Locate and identify every blood parasite.
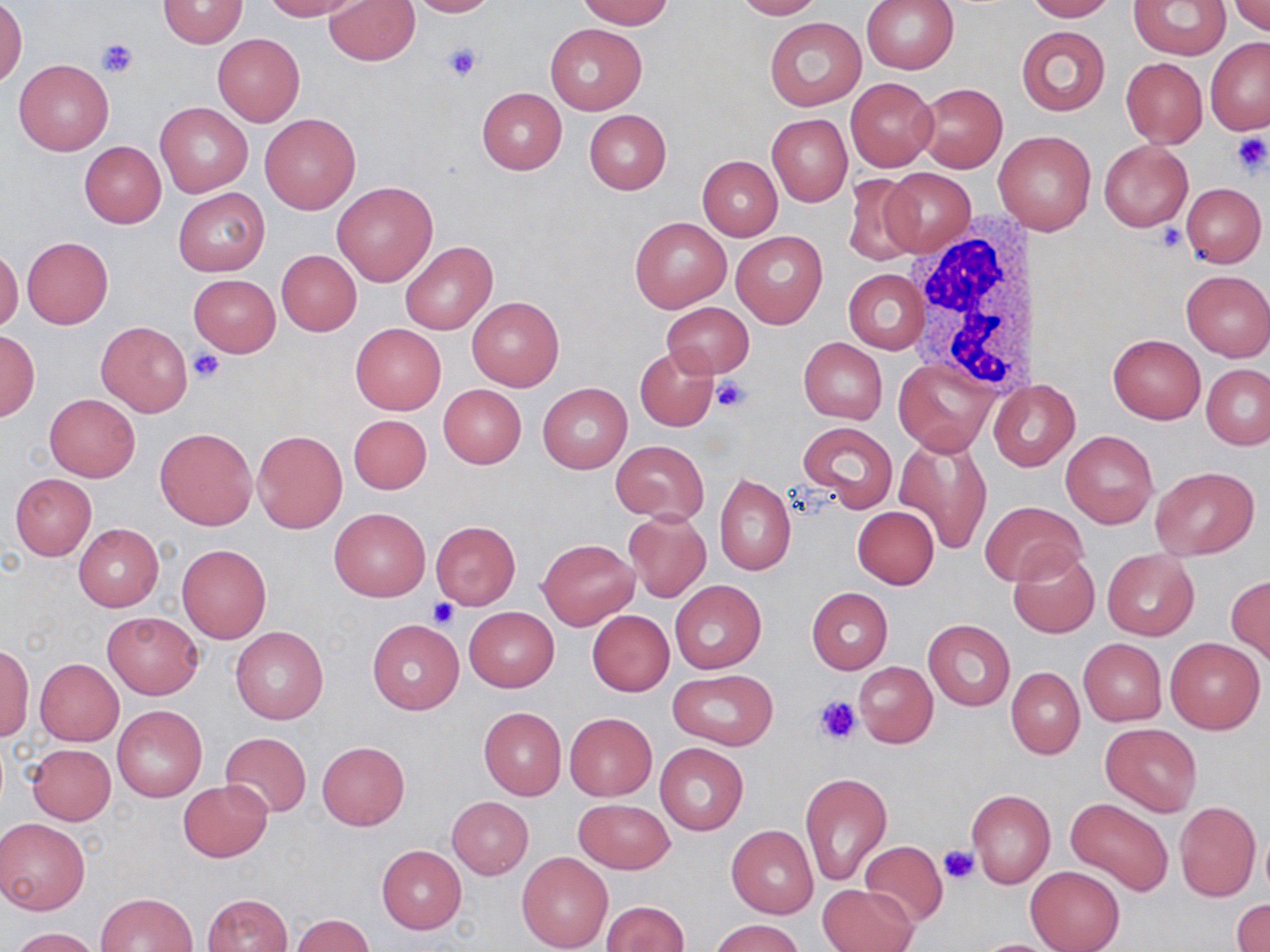

No blood parasites seen.

Summary:
  - Coordinate format: approximate bounding boxes as [x1, y1, x2, y2] in pixels
  - Uninfected red blood cell locations: [158, 0, 248, 48], [261, 0, 362, 21], [323, 0, 420, 66], [403, 0, 498, 17], [577, 0, 673, 29], [731, 0, 823, 19], [861, 0, 960, 74], [1023, 0, 1116, 21], [1128, 0, 1231, 60], [0, 1, 26, 88], [1231, 1, 1270, 36], [764, 16, 867, 111], [544, 21, 647, 115], [1016, 25, 1110, 117], [212, 34, 304, 126], [1206, 37, 1270, 133], [1120, 57, 1208, 147], [14, 59, 112, 154], [846, 77, 939, 169], [915, 83, 1007, 172], [477, 87, 566, 175], [156, 103, 251, 196], [583, 109, 671, 194], [260, 112, 361, 214], [767, 113, 852, 206], [997, 130, 1095, 235], [79, 141, 166, 228], [1099, 141, 1193, 231], [697, 155, 783, 240], [881, 167, 976, 256], [842, 174, 922, 269], [332, 181, 438, 287], [1181, 181, 1266, 267], [174, 188, 269, 277], [629, 216, 731, 313], [732, 232, 827, 328], [22, 237, 113, 328], [400, 241, 497, 335], [0, 248, 22, 332], [277, 250, 362, 336], [844, 269, 927, 354], [1181, 271, 1270, 361], [188, 274, 280, 356], [465, 296, 564, 391], [661, 301, 754, 377], [96, 320, 193, 417], [351, 323, 445, 414], [0, 330, 38, 419], [1108, 335, 1205, 423], [799, 338, 887, 422], [635, 346, 720, 432], [895, 360, 995, 453], [1201, 363, 1270, 450], [997, 378, 1077, 472], [538, 383, 632, 473], [438, 384, 526, 469], [45, 394, 139, 481], [348, 414, 432, 495], [798, 421, 897, 511], [156, 427, 256, 530], [252, 429, 347, 533], [1061, 430, 1158, 528], [893, 433, 992, 554], [611, 440, 709, 523], [1150, 465, 1259, 560], [714, 473, 795, 577], [9, 474, 96, 560], [981, 501, 1085, 586], [852, 506, 939, 588], [330, 508, 430, 601], [624, 510, 711, 602], [429, 521, 522, 609], [73, 524, 163, 612], [538, 538, 639, 629], [177, 544, 272, 643], [1007, 547, 1100, 639], [1101, 548, 1199, 640], [1227, 576, 1270, 664], [670, 580, 766, 674], [806, 587, 893, 673], [464, 607, 558, 692], [588, 610, 674, 695], [103, 612, 203, 699], [368, 618, 464, 715], [923, 620, 1015, 709], [231, 625, 329, 725], [1165, 637, 1265, 733], [1079, 639, 1167, 726], [1, 644, 33, 740], [35, 659, 123, 745], [854, 661, 938, 748], [1006, 667, 1084, 759], [667, 669, 779, 750], [113, 706, 207, 801], [478, 707, 566, 800], [564, 712, 657, 801], [1100, 722, 1202, 816], [219, 731, 312, 818], [317, 742, 409, 831], [26, 743, 116, 825], [655, 743, 748, 834], [800, 772, 891, 885], [180, 781, 271, 861], [966, 788, 1055, 888], [446, 796, 534, 879], [1065, 797, 1173, 895], [574, 799, 674, 873], [1175, 801, 1260, 901], [0, 817, 90, 914], [727, 825, 818, 918], [859, 841, 949, 928], [377, 845, 466, 933], [517, 852, 614, 952], [1025, 866, 1123, 952], [818, 883, 915, 952], [97, 892, 198, 952], [203, 893, 293, 952], [1231, 898, 1270, 952], [599, 901, 689, 951], [290, 914, 374, 951], [712, 918, 805, 952], [8, 926, 103, 952], [968, 938, 1068, 951]
  - White blood cell locations: [907, 216, 1036, 393]
  - Platelet locations: [95, 37, 138, 78], [443, 41, 484, 83], [1230, 132, 1268, 177], [1155, 224, 1186, 252], [189, 348, 226, 384], [711, 375, 753, 412], [427, 599, 459, 629], [813, 696, 862, 745], [937, 843, 979, 884]
  - Slide-level diagnosis: no evidence of blood parasites
  - Stain: May-Grünwald-Giemsa
  - Magnification: 1000x
  - Preparation: thin blood film
  - Modality: optical microscopy
  - Image size: 1270×952 pixels
  - Field of view: one of a larger specimen